Point out every Plasmodium parasite and every leukocyte.
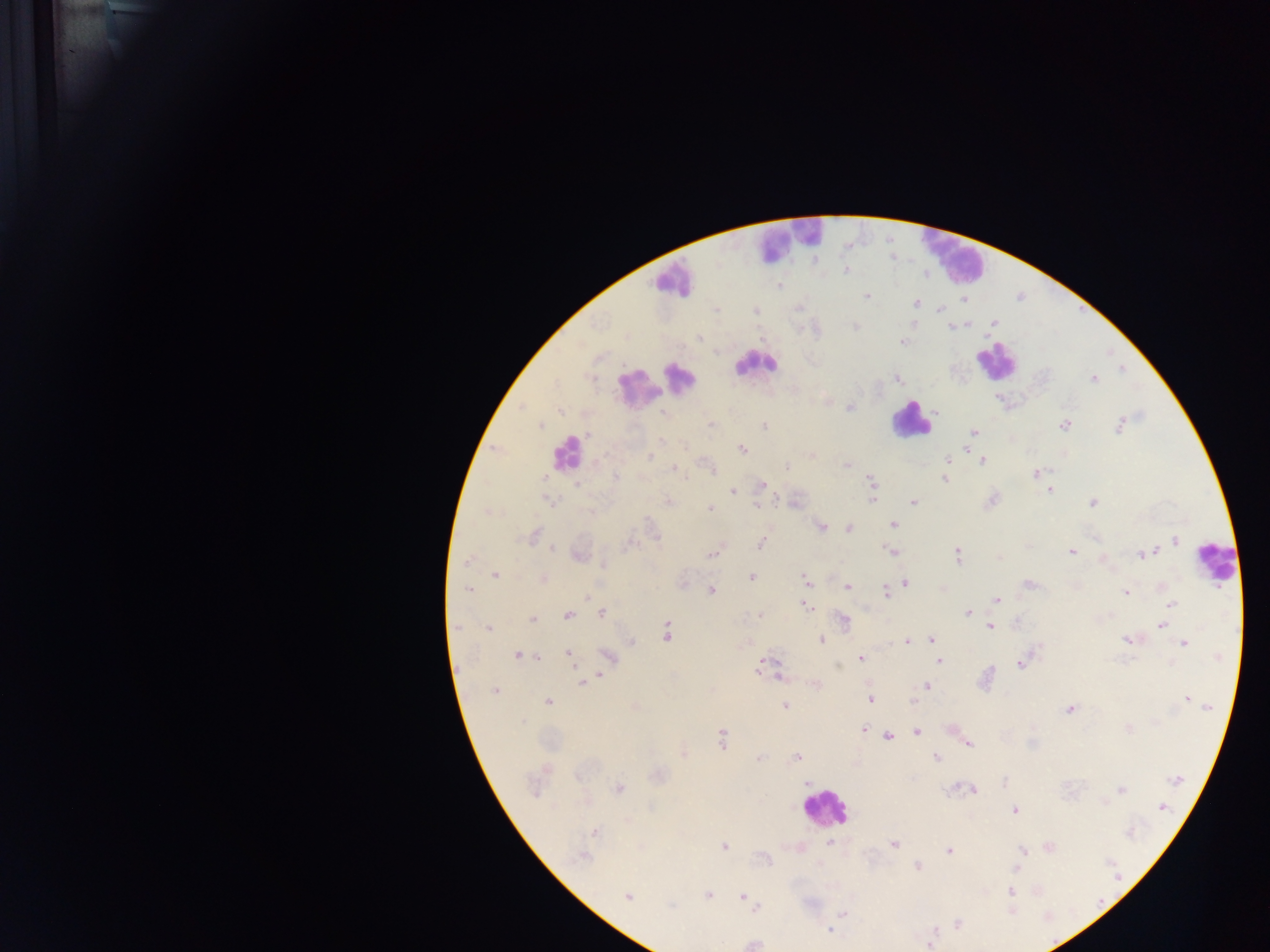
Approximate centers as x y in pixels.
Plasmodium parasites: 844 269; 779 286; 867 296; 963 299; 916 303; 940 309; 756 311; 993 321; 914 323; 855 326; 949 327; 699 337; 902 342; 1121 370; 1092 378; 896 379; 851 407; 1064 425; 1119 425; 539 426; 709 426; 764 426; 973 432; 661 440; 742 449; 964 450; 812 454; 649 456; 946 461; 982 461; 847 464; 787 466; 673 469; 1035 472; 614 477; 686 479; 945 479; 872 482; 576 485; 761 486; 1050 489; 733 490; 991 499; 547 500; 795 501; 872 501; 667 502; 913 502; 1091 502; 757 504; 710 508; 488 512; 893 525; 820 527; 849 528; 533 535; 1174 541; 761 543; 630 544; 552 549; 1071 551; 713 552; 892 552; 579 554; 957 554; 1143 554; 1101 559; 467 562; 495 575; 751 576; 542 579; 805 581; 681 582; 904 582; 1029 583; 847 587; 470 590; 711 590; 885 593; 1125 593; 996 600; 1171 605; 806 606; 602 612; 968 613; 758 614; 567 615; 533 619; 1164 619; 843 621; 1016 622; 1161 625; 990 626; 456 627; 488 628; 666 632; 821 639; 932 639; 1129 639; 906 640; 630 641; 1184 643; 569 654; 518 655; 609 657; 861 658; 938 661; 1020 663; 761 665; 773 673; 778 676; 592 678; 582 681; 815 684; 925 686; 495 691; 1187 698; 870 699; 548 701; 912 702; 635 706; 784 706; 1069 709; 1128 727; 951 728; 862 729; 916 731; 888 734; 722 740; 967 743; 684 753; 759 757; 796 757; 935 757; 657 776; 1177 779; 1004 782; 536 785; 618 788; 972 789; 1121 789; 1162 806; 1014 810; 594 833; 829 843; 893 844; 724 846; 1048 846; 948 851; 1023 851; 581 856; 916 867; 1016 869; 1011 891; 708 894; 628 897; 743 897; 756 909; 1010 909; 842 913; 957 924; 829 930; 751 943; 929 943.
Leukocytes: 788 239; 956 260; 672 280; 997 361; 756 363; 679 376; 661 381; 635 386; 912 420; 567 453; 1216 562; 824 808.

Summary:
  - Image size: 1270×952 pixels
  - Country: Ghana
  - Field of view: single
  - Capture: mobile-phone photograph through a microscope
  - Preparation: thick blood smear